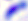

{
  "identification": "Toxoplasma gondii",
  "modality": "photomicrograph",
  "magnification": "400x"
}